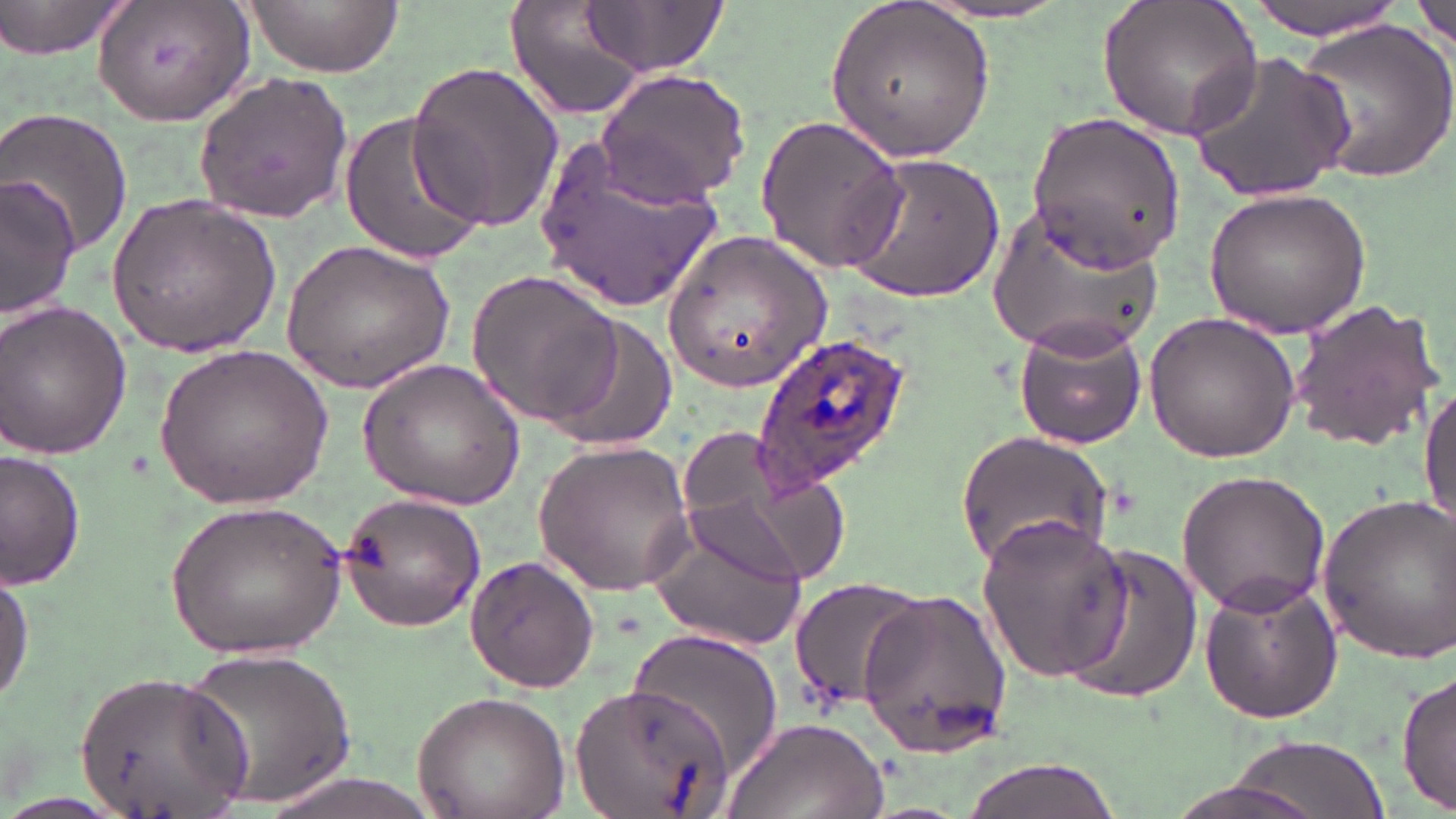
Summary:
  - Coordinate format: approximate bounding boxes as [x1, y1, x2, y2] in pixels
  - Plasmodium ovale-infected red blood cell locations: [754, 331, 911, 487]
  - Uninfected red blood cell locations: [0, 0, 126, 58], [502, 0, 658, 119], [825, 0, 998, 163], [1097, 0, 1264, 141], [1244, 0, 1410, 40], [90, 1, 255, 124], [242, 1, 403, 77], [577, 1, 730, 78], [1414, 1, 1455, 52], [1295, 18, 1455, 187], [1184, 49, 1356, 205], [406, 61, 564, 232], [596, 67, 750, 207], [192, 71, 353, 224], [0, 107, 134, 260], [338, 109, 487, 267], [1029, 109, 1187, 270], [754, 114, 911, 274], [537, 126, 729, 314], [841, 153, 1006, 304], [2, 176, 81, 319], [1204, 187, 1371, 336], [105, 191, 281, 354], [990, 199, 1165, 354], [663, 230, 832, 395], [279, 237, 455, 393], [465, 269, 627, 428], [1288, 297, 1445, 451], [0, 301, 132, 461], [1142, 311, 1302, 461], [543, 317, 678, 453], [1013, 318, 1147, 449], [153, 344, 333, 510], [358, 356, 525, 512], [1420, 381, 1456, 532], [953, 430, 1113, 568], [675, 431, 839, 591], [532, 440, 697, 594], [1, 450, 85, 589], [1176, 470, 1331, 619], [337, 489, 487, 635], [1313, 493, 1454, 667], [167, 498, 346, 660], [975, 511, 1133, 684], [645, 512, 808, 653], [1063, 544, 1204, 705], [466, 552, 599, 694], [0, 562, 34, 712], [1196, 574, 1345, 725], [787, 577, 926, 709], [859, 588, 1013, 758], [620, 626, 784, 774], [185, 643, 359, 811], [77, 670, 251, 815], [1397, 671, 1456, 813], [573, 680, 734, 819], [410, 690, 570, 819], [721, 716, 888, 819], [1215, 734, 1391, 818], [954, 756, 1129, 819], [239, 770, 465, 819], [1161, 777, 1328, 819]
  - Slide-level diagnosis: Plasmodium ovale
  - Stain: May-Grünwald-Giemsa
  - Modality: light microscopy
  - Image size: 1456×819 pixels
  - Preparation: thin blood smear
  - Magnification: 1000x
  - Field of view: one of a larger specimen